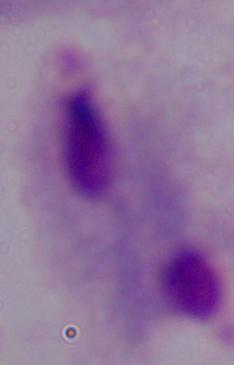
magnification = 1000x
identification = trichomonad
modality = photomicrograph